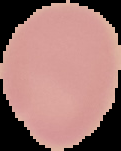

Summary:
  - Preparation: thin blood smear
  - Image type: segmented cell region with the area outside set to black
  - Malaria status: uninfected
  - Image size: 121×151 pixels